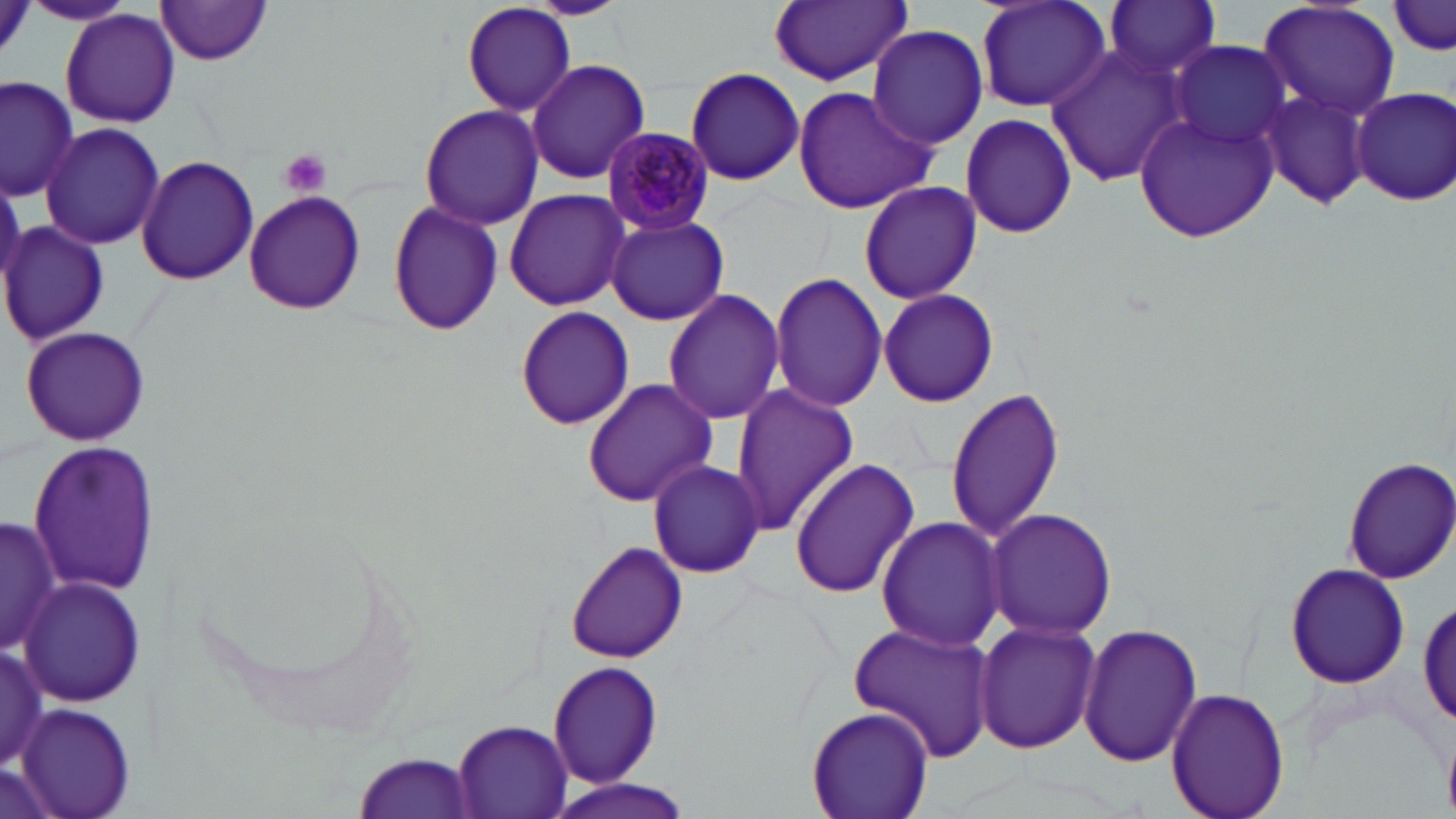

slide-level diagnosis = Plasmodium malariae
preparation = thin blood film
platelet locations = approximate bounding boxes as (x1,y1)-(x2,y2) corner pairs in pixels: (277,149)-(332,199)
field of view = one of a larger specimen
modality = optical microscopy
Plasmodium malariae-infected red blood cell locations = approximate bounding boxes as (x1,y1)-(x2,y2) corner pairs in pixels: (602,126)-(716,237)
magnification = 1000x
image size = 1456×819 pixels
stain = May-Grünwald-Giemsa
uninfected red blood cell locations = approximate bounding boxes as (x1,y1)-(x2,y2) corner pairs in pixels: (155,0)-(275,66), (461,0)-(577,115), (522,0)-(631,19), (972,0)-(1111,115), (1101,0)-(1222,83), (24,1)-(133,28), (770,1)-(912,86), (1258,1)-(1400,120), (1388,3)-(1455,58), (60,9)-(182,129), (866,24)-(989,149), (1171,41)-(1291,149), (1044,46)-(1189,185), (525,58)-(652,183), (684,66)-(806,186), (2,76)-(80,201), (1257,85)-(1376,211), (790,86)-(937,214), (1350,86)-(1456,206), (418,103)-(546,230), (1134,108)-(1281,241), (959,112)-(1077,240), (38,123)-(164,250), (137,155)-(260,285), (859,180)-(983,304), (503,189)-(630,311), (243,190)-(365,314), (387,202)-(503,337), (605,215)-(730,326), (0,221)-(110,348), (769,272)-(888,414), (662,288)-(786,427), (877,288)-(999,408), (513,306)-(634,431), (21,326)-(148,445), (580,377)-(717,506), (731,384)-(860,534), (946,386)-(1063,544), (29,442)-(157,595), (789,457)-(919,599), (1342,457)-(1456,584), (647,461)-(765,578), (984,508)-(1118,642), (174,509)-(422,737), (1,515)-(62,654), (875,515)-(1005,652), (567,542)-(686,662), (1283,563)-(1412,690), (17,576)-(147,705), (1418,591)-(1456,734), (973,618)-(1101,757), (846,621)-(999,764), (1077,621)-(1204,768), (0,635)-(53,774), (548,659)-(664,791), (1166,685)-(1289,819), (16,705)-(138,819), (806,706)-(932,819), (451,719)-(574,819), (350,751)-(480,818), (545,778)-(698,819)